Look for Plasmodium parasites.
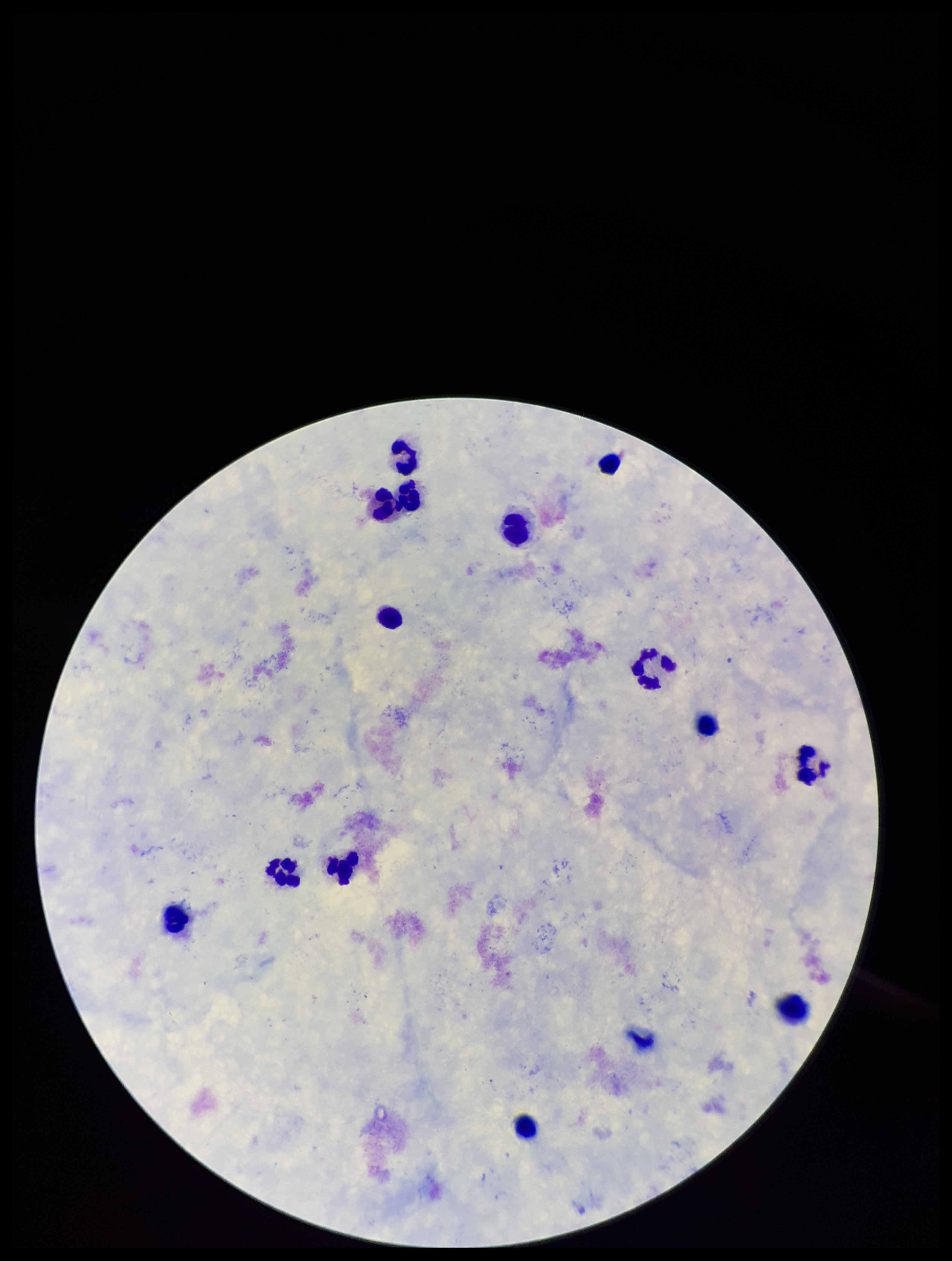
None identified.

Summary:
  - Parasite count: 0
  - Capture: smartphone photograph through the microscope eyepiece
  - Image size: 952×1261 pixels
  - Field of view: single
  - Patient malaria status: negative
  - Stain: Giemsa
  - Preparation: thick smear
  - Leukocyte count: 14